Describe the morphology of the erythrocytes.
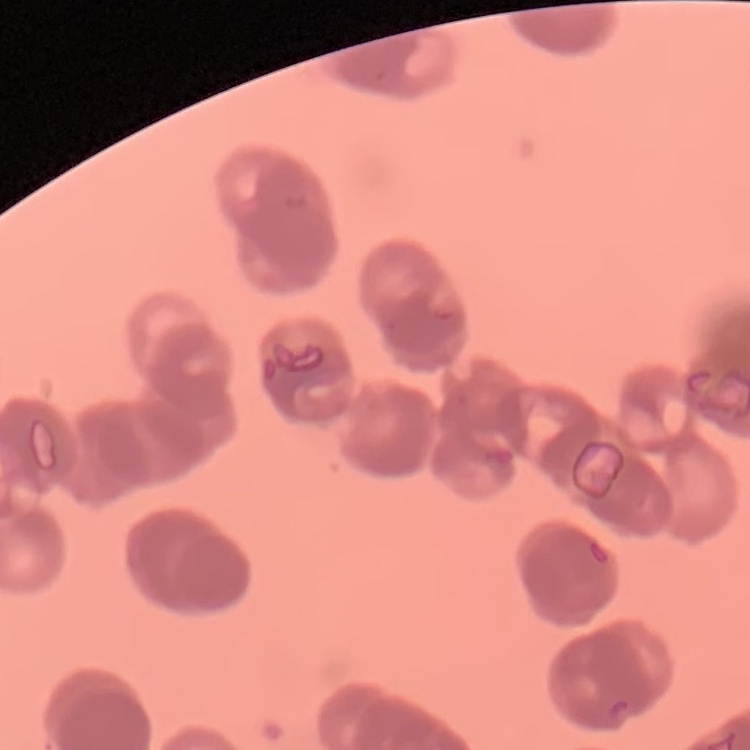

They show rouleaux formation.

Summary:
  - Preparation: thin peripheral smear
  - Image type: square crop of a larger photomicrograph
  - Stain: Field's or Giemsa